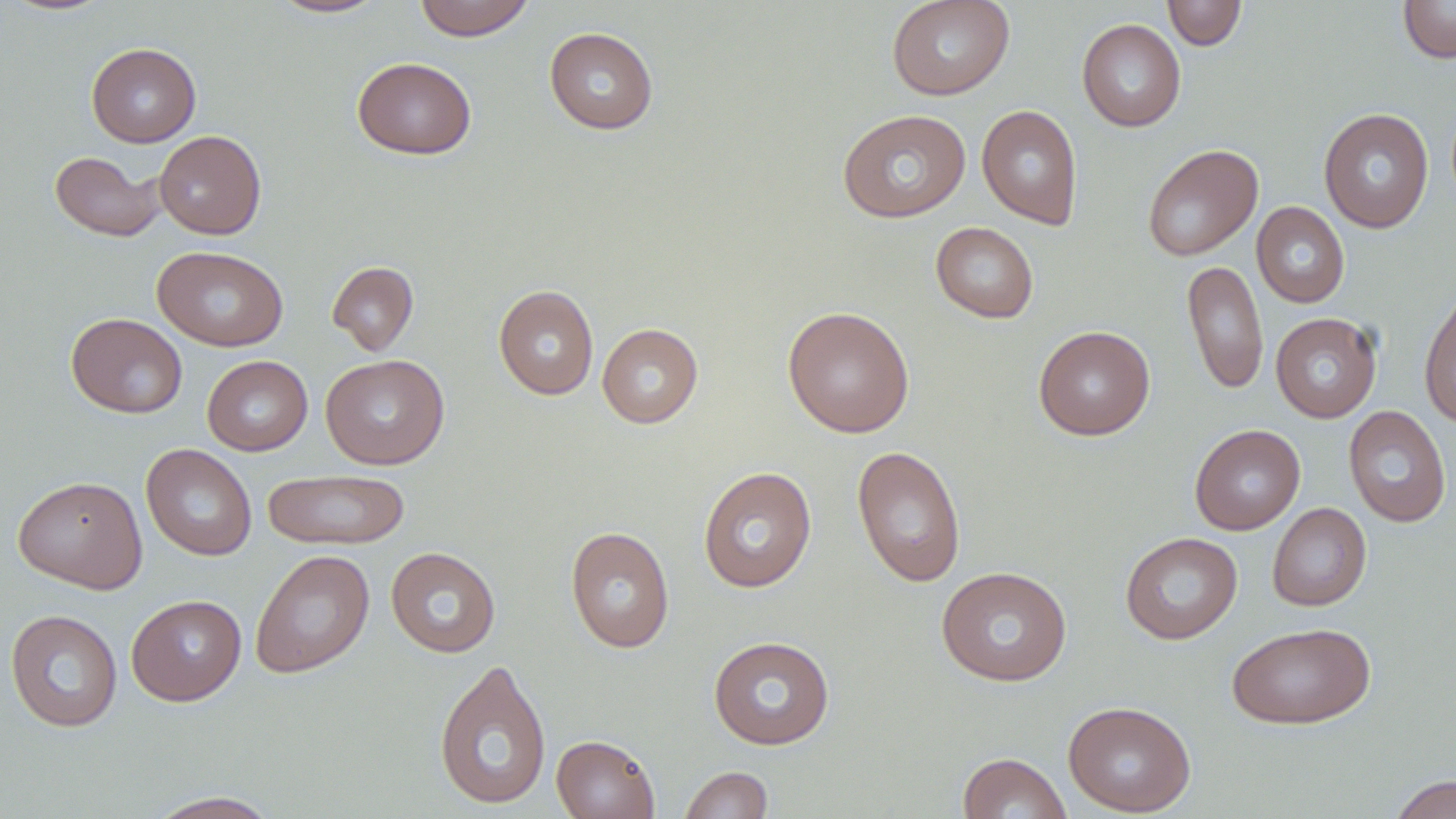 Approximate bounding boxes as [x1, y1, x2, y2] in pixels. Uninfected red blood cell locations: [1, 0, 117, 17], [269, 0, 389, 19], [413, 0, 535, 41], [886, 0, 1016, 100], [1162, 0, 1247, 51], [1398, 0, 1456, 64], [1076, 18, 1186, 132], [544, 26, 659, 135], [86, 42, 201, 147], [352, 56, 477, 160], [977, 104, 1083, 230], [1318, 108, 1434, 233], [837, 109, 972, 222], [154, 130, 266, 239], [1141, 144, 1263, 261], [49, 150, 166, 242], [1252, 202, 1350, 308], [931, 221, 1039, 324], [152, 245, 288, 351], [1182, 260, 1268, 396], [327, 261, 419, 356], [493, 284, 599, 400], [1419, 288, 1456, 429], [782, 305, 914, 438], [1270, 312, 1382, 422], [66, 313, 188, 419], [597, 323, 703, 428], [1033, 325, 1156, 440], [320, 354, 449, 469], [202, 355, 312, 456], [1343, 405, 1451, 527], [1190, 423, 1305, 535], [141, 444, 257, 561], [852, 445, 967, 587], [698, 467, 817, 592], [263, 468, 411, 550], [13, 475, 147, 593], [1267, 503, 1372, 611], [565, 525, 675, 653], [1120, 532, 1243, 644], [385, 546, 501, 658], [250, 549, 374, 678], [936, 566, 1073, 686], [126, 594, 246, 706], [5, 609, 122, 732], [1227, 622, 1376, 729], [708, 635, 835, 750], [433, 657, 552, 810], [1063, 700, 1196, 816], [551, 734, 659, 819], [958, 752, 1072, 818], [679, 766, 773, 818], [1387, 773, 1456, 818], [145, 790, 283, 818]. Slide-level diagnosis: no evidence of blood parasites. Thin blood film. One field of a larger specimen. Optical microscopy. May-Grünwald-Giemsa-stained preparation. Image is 1456×819 pixels. Captured at 1000x magnification.